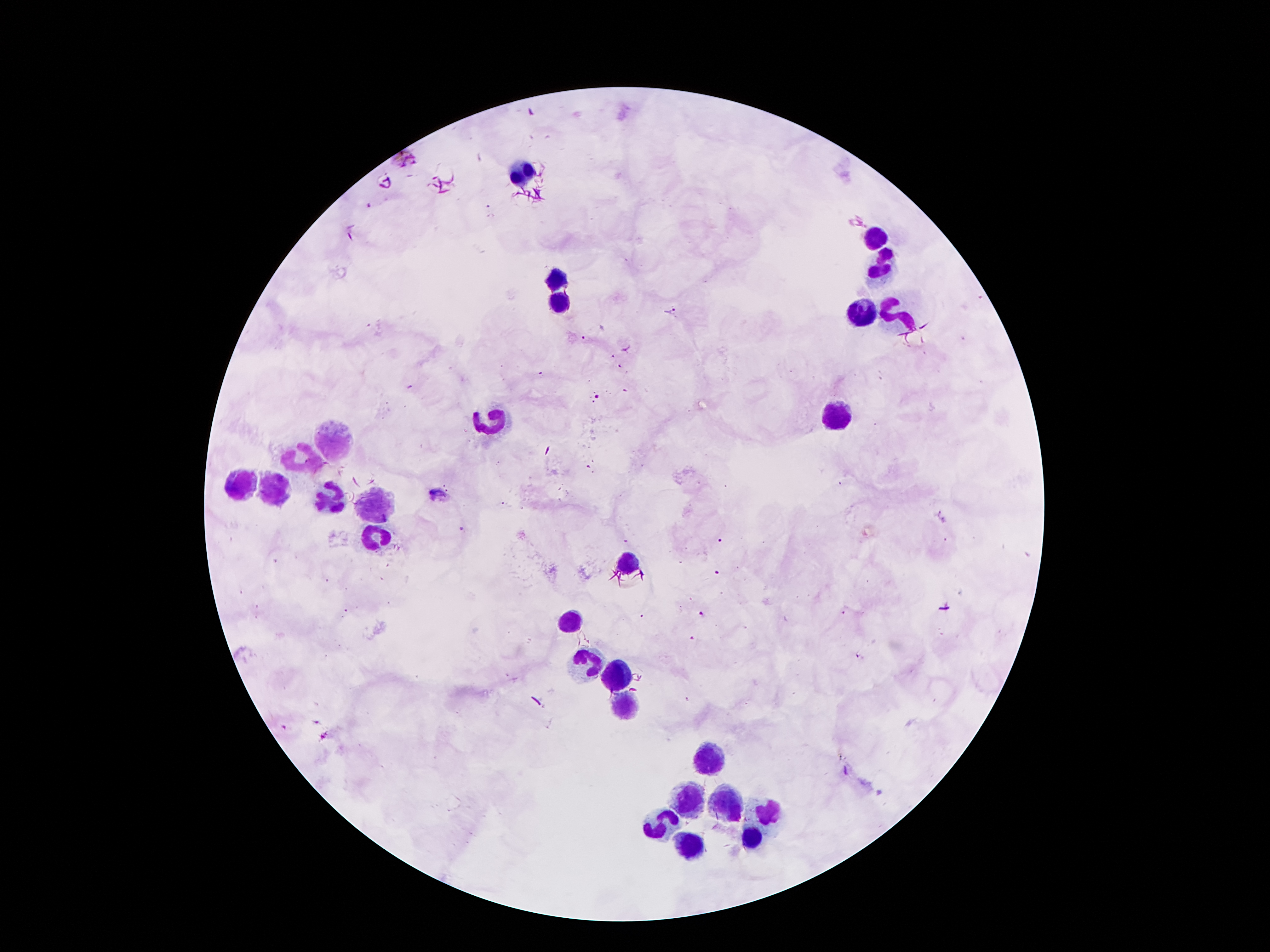

coordinate format = approximate object centers, in pixels from the top-left corner
Plasmodium parasite locations = (x=670, y=312), (x=586, y=337), (x=598, y=398), (x=438, y=492), (x=721, y=540), (x=717, y=573), (x=703, y=615), (x=694, y=639), (x=861, y=656), (x=687, y=699)
leukocyte locations = (x=522, y=169), (x=879, y=237), (x=883, y=264), (x=559, y=278), (x=559, y=300), (x=865, y=312), (x=902, y=314), (x=838, y=416), (x=493, y=418), (x=334, y=441), (x=302, y=459), (x=238, y=486), (x=270, y=491), (x=327, y=502), (x=375, y=505), (x=375, y=539), (x=627, y=564), (x=572, y=620), (x=584, y=659), (x=620, y=670), (x=625, y=704), (x=709, y=761), (x=688, y=800), (x=727, y=804), (x=768, y=816), (x=663, y=825), (x=752, y=841), (x=688, y=850)
field of view = one from this slide
preparation = thick blood smear
capture = smartphone camera through the microscope eyepiece
patient malaria status = infected with Plasmodium falciparum
image size = 1270×952 pixels
stain = Giemsa
magnification = 100x